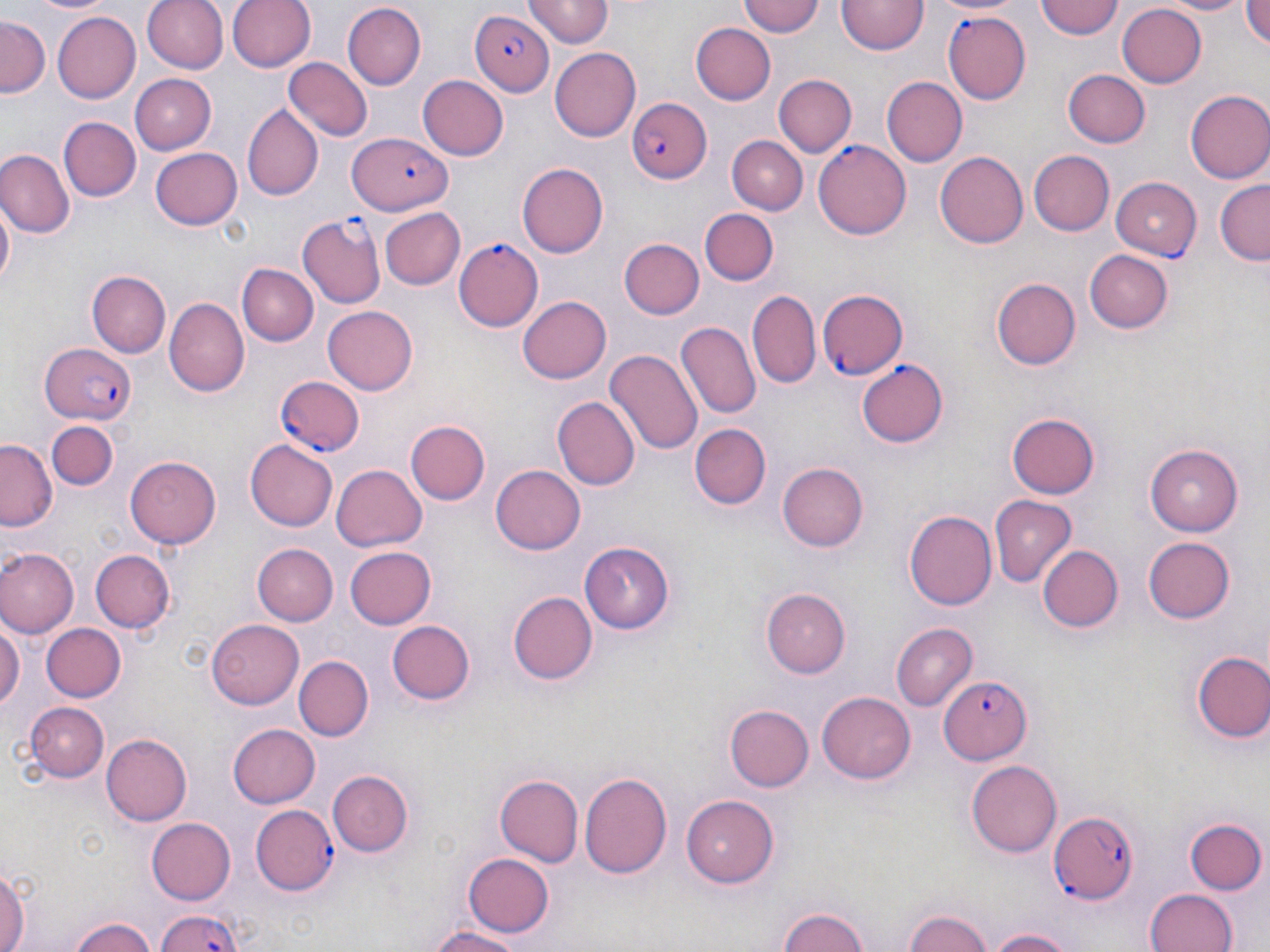

Summary:
  - Coordinate format: approximate bounding boxes as (x1,y1)-(x2,y2) corner pairs in pixels
  - Uninfected red blood cell locations: (29,0)-(112,15), (140,0)-(227,73), (228,0)-(315,74), (739,0)-(824,40), (928,0)-(1025,17), (1035,0)-(1122,40), (1159,0)-(1247,14), (525,1)-(612,47), (836,1)-(926,57), (1240,2)-(1267,51), (1117,3)-(1208,87), (344,4)-(426,88), (53,11)-(143,104), (0,17)-(47,99), (693,22)-(775,104), (549,44)-(640,138), (284,57)-(373,140), (1062,68)-(1149,147), (419,73)-(509,161), (130,74)-(217,154), (775,75)-(856,157), (882,77)-(967,167), (1185,89)-(1270,184), (243,104)-(322,201), (59,116)-(141,201), (727,136)-(807,213), (150,146)-(241,231), (935,150)-(1031,248), (1028,150)-(1114,235), (1,151)-(72,237), (516,162)-(609,259), (1215,181)-(1269,263), (0,191)-(15,299), (378,207)-(464,290), (700,209)-(779,285), (620,237)-(703,319), (1086,248)-(1172,334), (237,264)-(317,346), (87,271)-(170,357), (993,279)-(1081,369), (748,289)-(822,389), (516,296)-(611,383), (163,297)-(249,396), (323,305)-(419,394), (676,320)-(762,420), (605,349)-(703,456), (550,395)-(639,489), (1007,413)-(1100,500), (407,420)-(489,505), (49,422)-(115,491), (690,424)-(769,509), (0,439)-(56,530), (246,440)-(338,531), (1146,445)-(1244,535), (125,455)-(222,548), (331,463)-(427,553), (489,463)-(586,555), (778,463)-(868,551), (990,496)-(1077,587), (905,508)-(999,610), (1140,536)-(1235,625), (581,539)-(676,632), (252,542)-(337,624), (343,545)-(435,630), (1040,547)-(1122,632), (90,548)-(175,633), (0,549)-(77,639), (761,588)-(851,676), (509,592)-(599,685), (0,614)-(23,717), (207,620)-(303,710), (388,621)-(474,704), (44,623)-(126,703), (892,623)-(977,709), (1192,652)-(1270,743), (295,656)-(373,740), (817,690)-(914,784), (26,702)-(109,782), (724,704)-(813,791), (228,725)-(321,807), (102,733)-(192,825), (966,760)-(1063,856), (329,770)-(414,857), (580,771)-(672,878), (496,775)-(585,867), (682,795)-(780,888), (147,816)-(235,905), (1186,820)-(1267,896), (463,851)-(554,938), (0,864)-(28,952), (1144,888)-(1241,952), (777,906)-(872,952), (903,907)-(992,952), (69,916)-(156,952), (422,924)-(525,952), (984,927)-(1085,952)
  - Plasmodium falciparum-infected red blood cell locations: (471,9)-(553,98), (942,12)-(1032,105), (628,97)-(712,185), (348,138)-(454,213), (813,139)-(912,236), (1111,177)-(1203,260), (299,213)-(385,308), (453,236)-(543,330), (818,287)-(908,379), (41,346)-(135,426), (855,359)-(949,449), (276,376)-(367,457), (940,675)-(1030,764), (251,804)-(338,894), (1045,809)-(1140,901), (147,906)-(248,952)
  - Slide-level diagnosis: Plasmodium falciparum
  - Preparation: thin blood film
  - Modality: optical microscopy
  - Magnification: 1000x
  - Stain: May-Grünwald-Giemsa
  - Image size: 1270×952 pixels
  - Field of view: one of a larger specimen